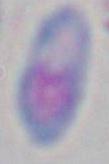

Summary:
  - Modality: photomicrograph
  - Identification: Toxoplasma gondii
  - Magnification: 1000x